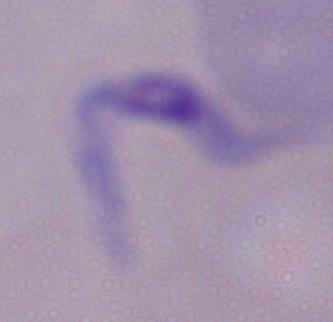
modality = photomicrograph
identification = trypanosome
magnification = 1000x